Describe the morphology of the red blood cells.
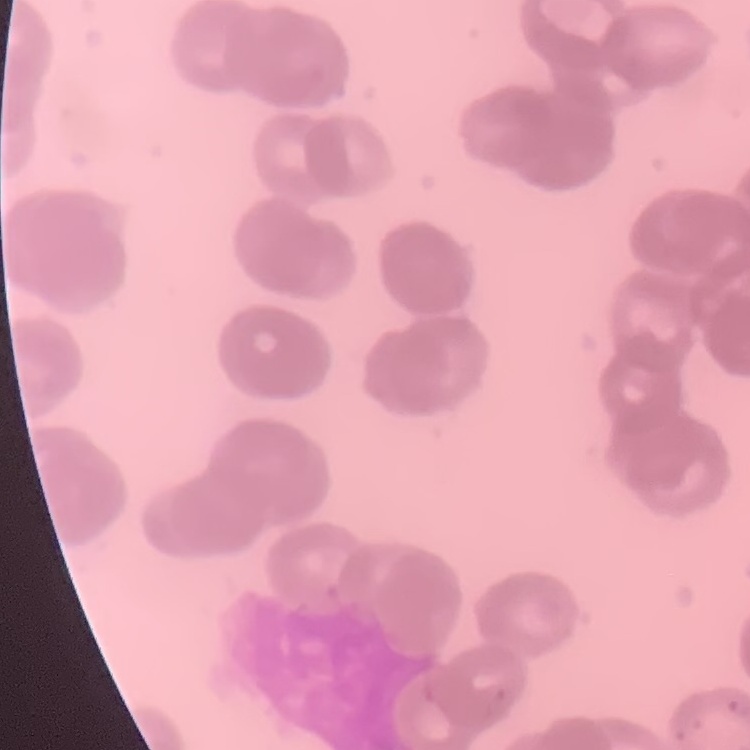
They show rouleaux formation.

stain = Field's or Giemsa
image type = one tile cut from a larger photomicrograph
preparation = thin blood film